Assess this cell for malaria.
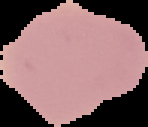

Uninfected.

image_size: 148×127 pixels
preparation: thin blood smear
image_type: segmented cell region with the area outside set to black